Classify this cell by malaria status.
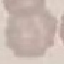
It is uninfected.

capture: smartphone through the microscope eyepiece
stain: Giemsa
image_type: automatically extracted cell patch, resized to 64 × 64 pixels
preparation: thin blood smear